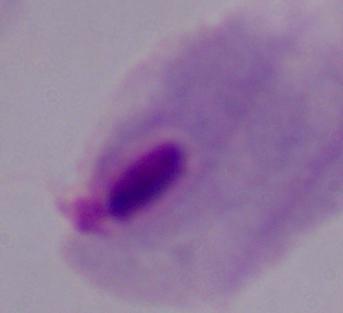

modality = micrograph
identification = trichomonad
magnification = 1000x